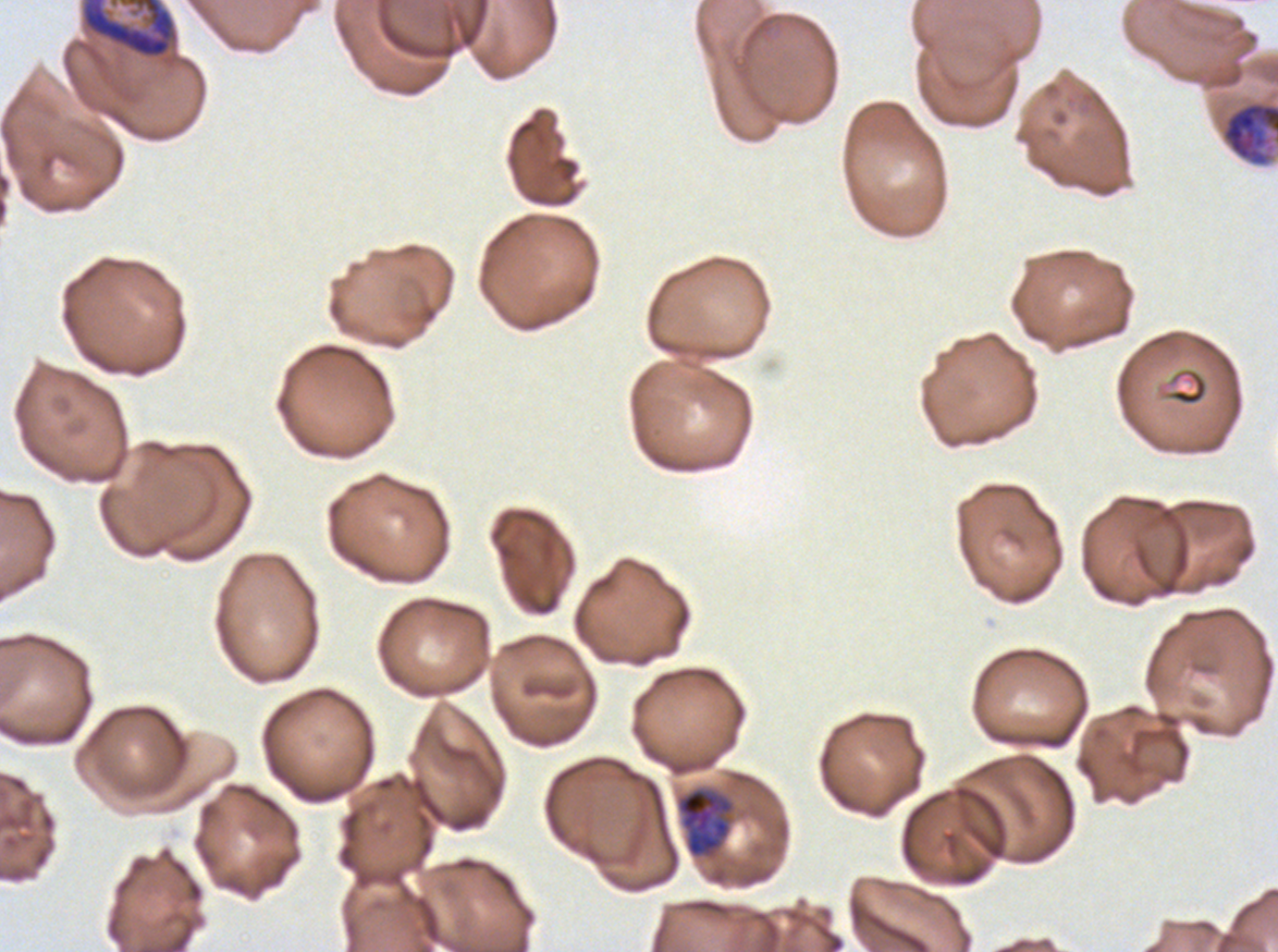
field_of_view: sub-image separated from a larger composite
image_size: 1278×952 pixels
specimen: Plasmodium falciparum from a patient in The Gambia, cultured ex vivo for 24 to 48 hours
early_schizont_locations: 'approximate bounding boxes as (x1, y1, x2, y2) in pixels: (80, 0, 180, 68), (1221, 100, 1277, 167)'
stain: Giemsa
preparation: thin blood film
life_cycle_stages_observed: late trophozoite, early schizont
late_trophozoite_locations: 'approximate bounding boxes as (x1, y1, x2, y2) in pixels: (676, 787, 735, 859)'